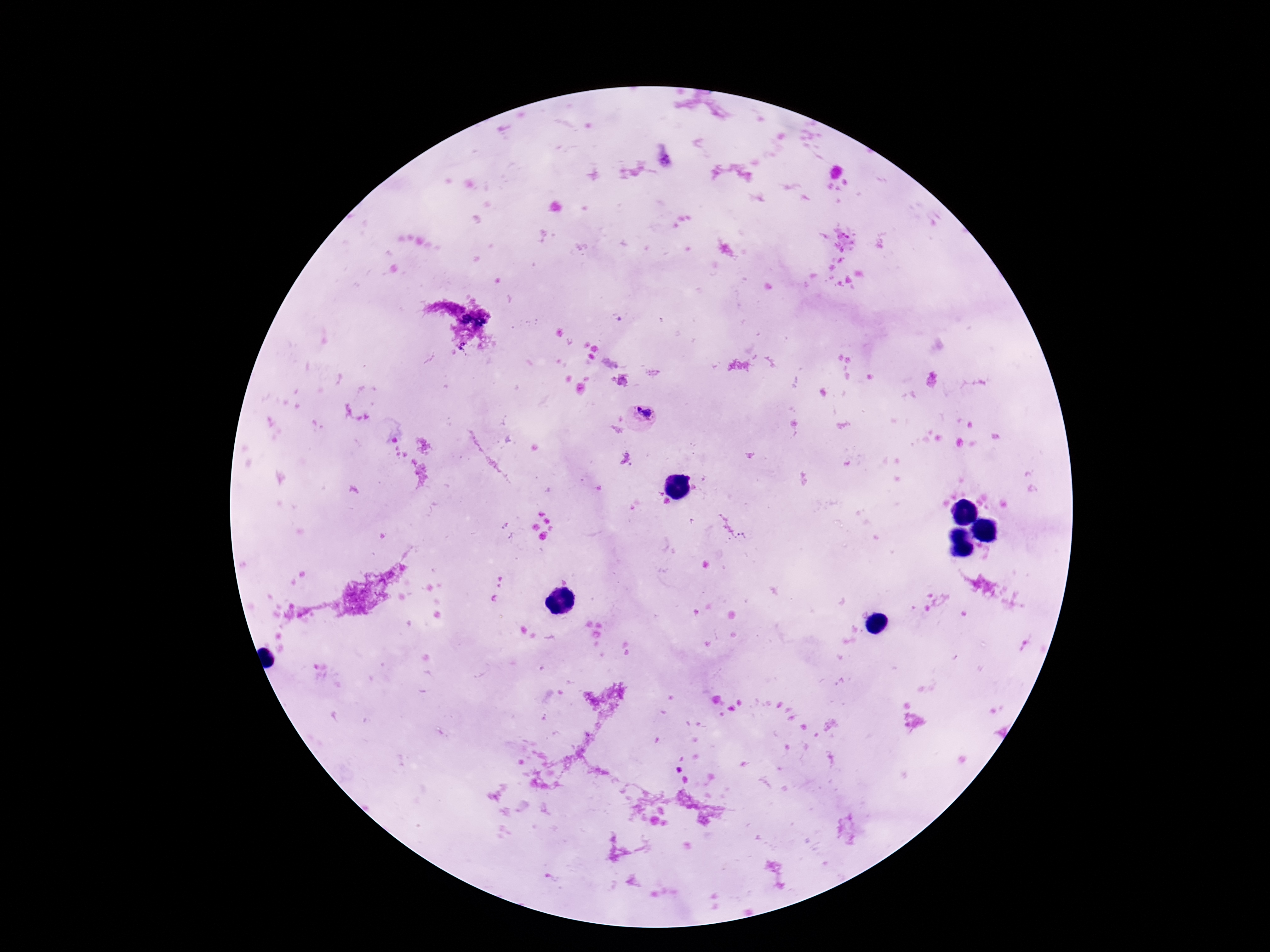
Approximate centers as [x, y] in pixels. Plasmodium parasite locations: [643, 417]. Giemsa stain. Patient malaria status: positive. Thick blood smear. One field from this slide. Image is 1270×952 pixels. 100x magnification. Photographed through the microscope eyepiece with a smartphone camera.